Assess the morphology of the red blood cells.
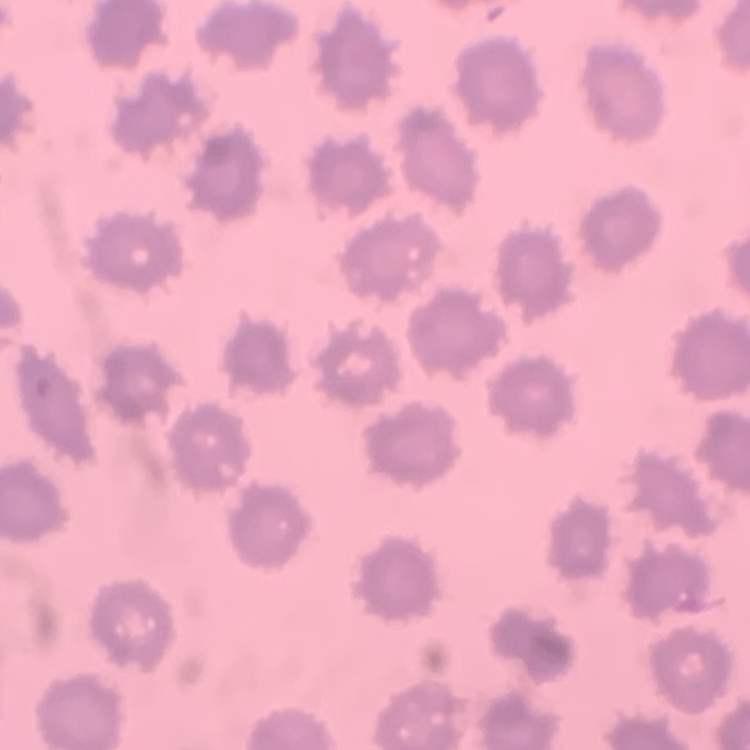
They show no rouleaux formation.

preparation: thin peripheral smear
stain: Field's or Giemsa
image_type: square crop of a larger photomicrograph